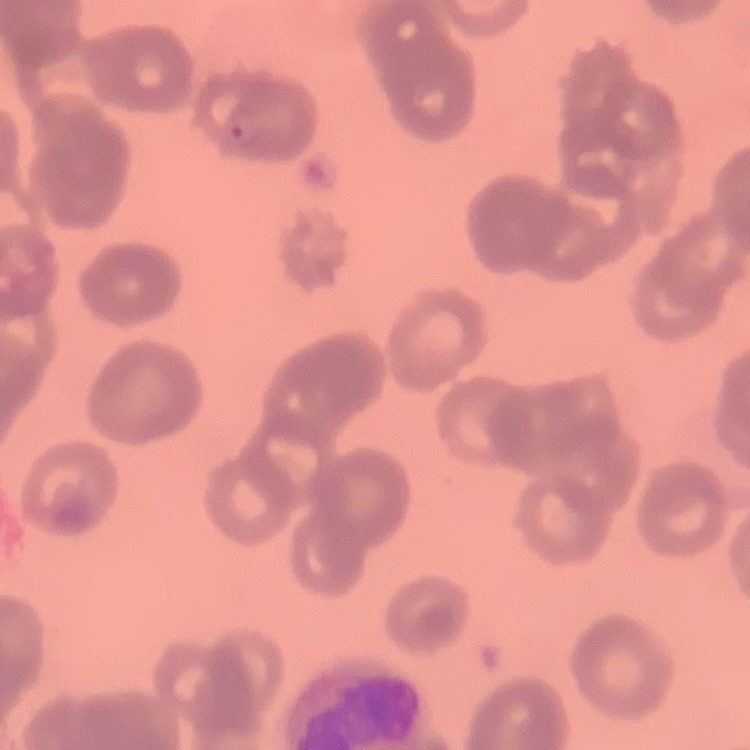
The erythrocytes exhibit rouleaux formation. Thin blood film. Square crop of a larger photomicrograph. Field's or Giemsa stain.